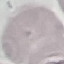

malaria status = uninfected
capture = smartphone through the microscope eyepiece
image type = cell patch, automatically extracted from a larger field of view and resized to 64 × 64 pixels
preparation = thin blood smear
stain = Giemsa